Describe the morphology of the red blood cells.
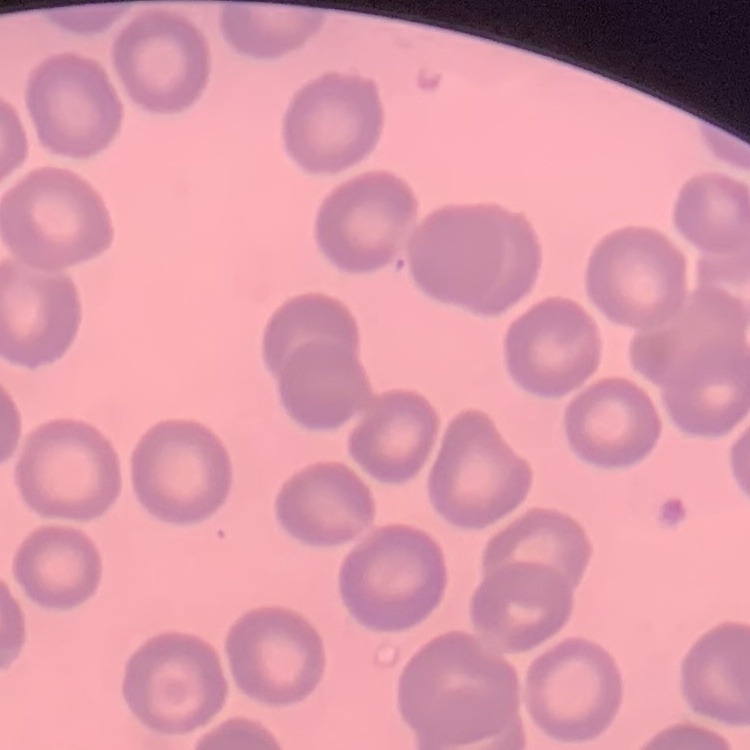

They show no rouleaux formation.

stain = Field's or Giemsa
preparation = thin blood film
image type = square crop of a larger photomicrograph